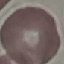 Result: no malaria parasites seen. Photographed with a smartphone camera at the microscope eyepiece. Thin smear of blood. Giemsa-stained preparation. Cell patch, automatically extracted from a larger field of view and resized to 64 × 64 pixels.